Classify this cell by malaria status.
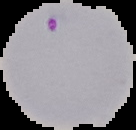

It is parasitized.

{
  "image_type": "cell region segmented out of the field of view; surrounding area masked to black",
  "preparation": "thin blood film",
  "image_size": "136×130 pixels"
}